Give the position of every Plasmodium parasite.
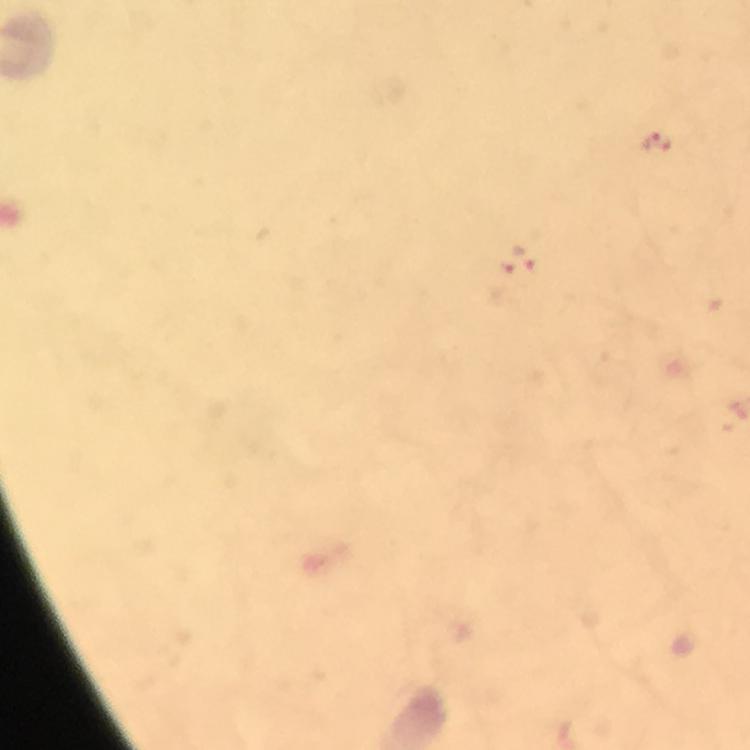

Approximate centers as [x, y] in pixels.
Plasmodium parasites: [655, 144], [517, 262].

From a malaria diagnostic workup. A crop from one field of view. Thick smear. Immersion oil was used. Giemsa-stained preparation. 100x magnification. Image is 750×750 pixels. Smartphone photograph taken through a microscope.